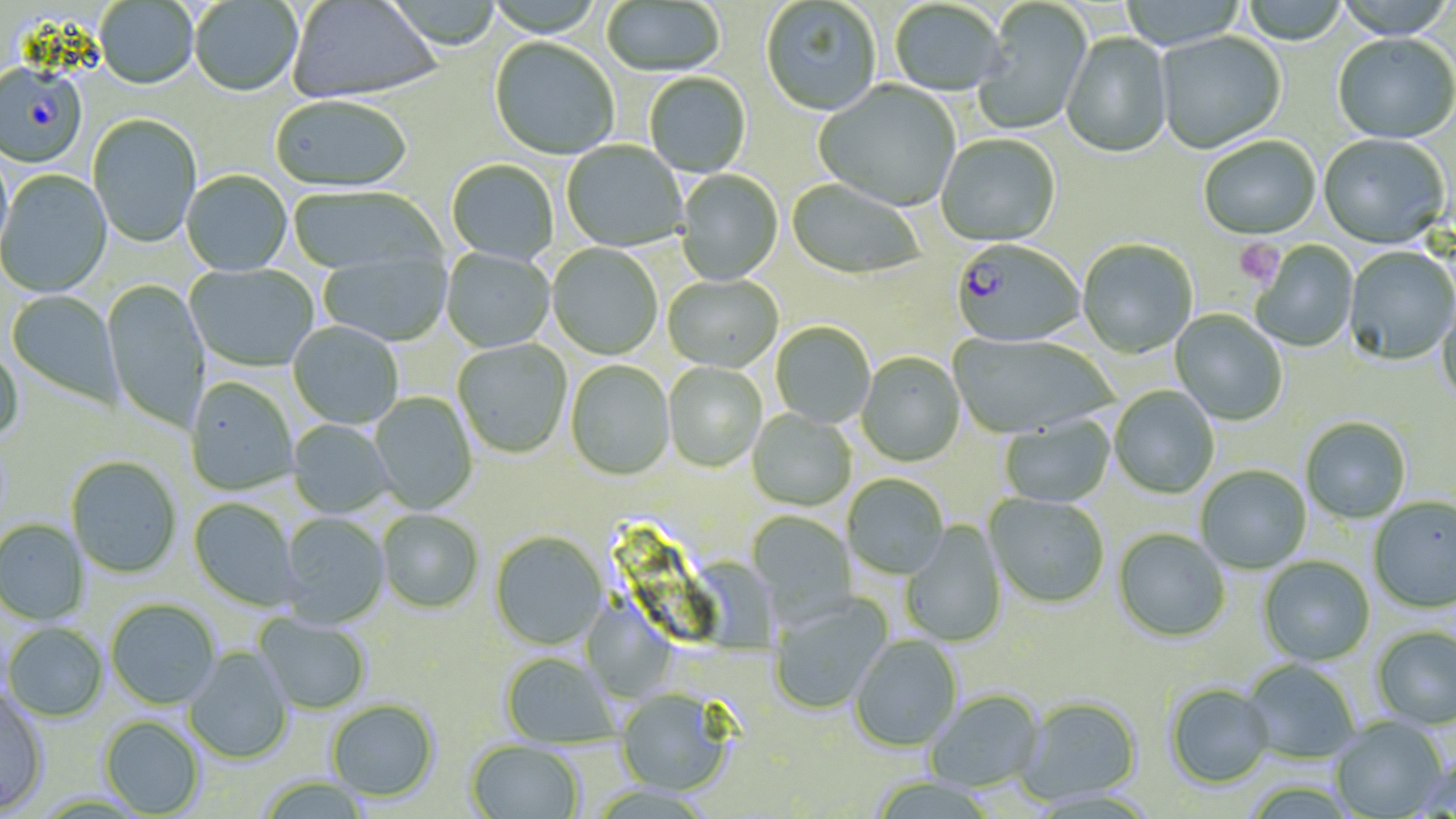

Summary:
  - Coordinate format: approximate bounding boxes as (x1, y1, x2, y2) in pixels
  - Uninfected red blood cell locations: (381, 0, 503, 52), (761, 0, 882, 118), (972, 0, 1093, 136), (1117, 0, 1247, 50), (1240, 0, 1349, 46), (1331, 0, 1455, 42), (94, 1, 199, 92), (190, 1, 303, 99), (288, 1, 443, 104), (601, 1, 726, 78), (889, 1, 1006, 99), (1156, 31, 1287, 155), (1061, 33, 1173, 160), (1333, 35, 1456, 146), (489, 39, 619, 161), (644, 74, 751, 178), (814, 80, 960, 213), (270, 97, 412, 195), (88, 115, 202, 249), (935, 135, 1060, 248), (1318, 135, 1451, 252), (1199, 136, 1321, 242), (561, 141, 687, 252), (0, 146, 14, 268), (447, 160, 559, 265), (0, 170, 112, 299), (675, 170, 784, 286), (181, 171, 293, 278), (786, 180, 923, 281), (288, 187, 444, 277), (1077, 240, 1198, 360), (1252, 240, 1358, 353), (547, 244, 662, 360), (1343, 247, 1455, 366), (441, 249, 555, 354), (318, 252, 451, 347), (185, 264, 319, 373), (663, 275, 783, 374), (102, 279, 210, 433), (6, 290, 123, 408), (1437, 298, 1456, 408), (1170, 311, 1287, 426), (288, 322, 403, 429), (771, 323, 875, 428), (948, 334, 1117, 441), (453, 339, 572, 459), (0, 342, 25, 445), (856, 353, 965, 467), (565, 361, 675, 481), (663, 362, 767, 473), (185, 378, 298, 496), (1109, 386, 1219, 499), (370, 392, 478, 513), (747, 409, 856, 512), (999, 416, 1116, 508), (287, 419, 395, 519), (1301, 419, 1411, 525), (65, 457, 182, 579), (1195, 465, 1311, 574), (843, 475, 949, 580), (983, 494, 1109, 609), (188, 497, 301, 612), (1368, 498, 1456, 614), (378, 510, 484, 614), (745, 510, 857, 626), (278, 513, 390, 628), (0, 519, 91, 625), (900, 522, 1008, 648), (1112, 530, 1230, 643), (490, 531, 608, 651), (681, 556, 788, 664), (1258, 556, 1375, 667), (768, 593, 893, 715), (105, 599, 220, 709), (580, 599, 677, 703), (253, 613, 371, 715), (3, 622, 109, 723), (1371, 626, 1456, 732), (850, 636, 963, 753), (184, 646, 294, 764), (500, 653, 620, 750), (1241, 659, 1360, 765), (1164, 684, 1274, 790), (0, 689, 49, 815), (615, 689, 734, 797), (926, 690, 1044, 793), (1015, 697, 1143, 807), (326, 699, 439, 803), (99, 716, 205, 817), (1330, 717, 1449, 818), (465, 739, 583, 819), (1415, 761, 1456, 818), (257, 776, 371, 819), (868, 777, 998, 819)
  - Platelet locations: (1234, 239, 1283, 287)
  - Plasmodium falciparum-infected red blood cell locations: (0, 66, 87, 169), (950, 241, 1084, 348)
  - Slide-level diagnosis: Plasmodium falciparum
  - Image size: 1456×819 pixels
  - Preparation: thin blood film
  - Stain: May-Grünwald-Giemsa
  - Modality: optical microscopy
  - Field of view: single
  - Magnification: 1000x